Outline each Plasmodium falciparum-infected red blood cell.
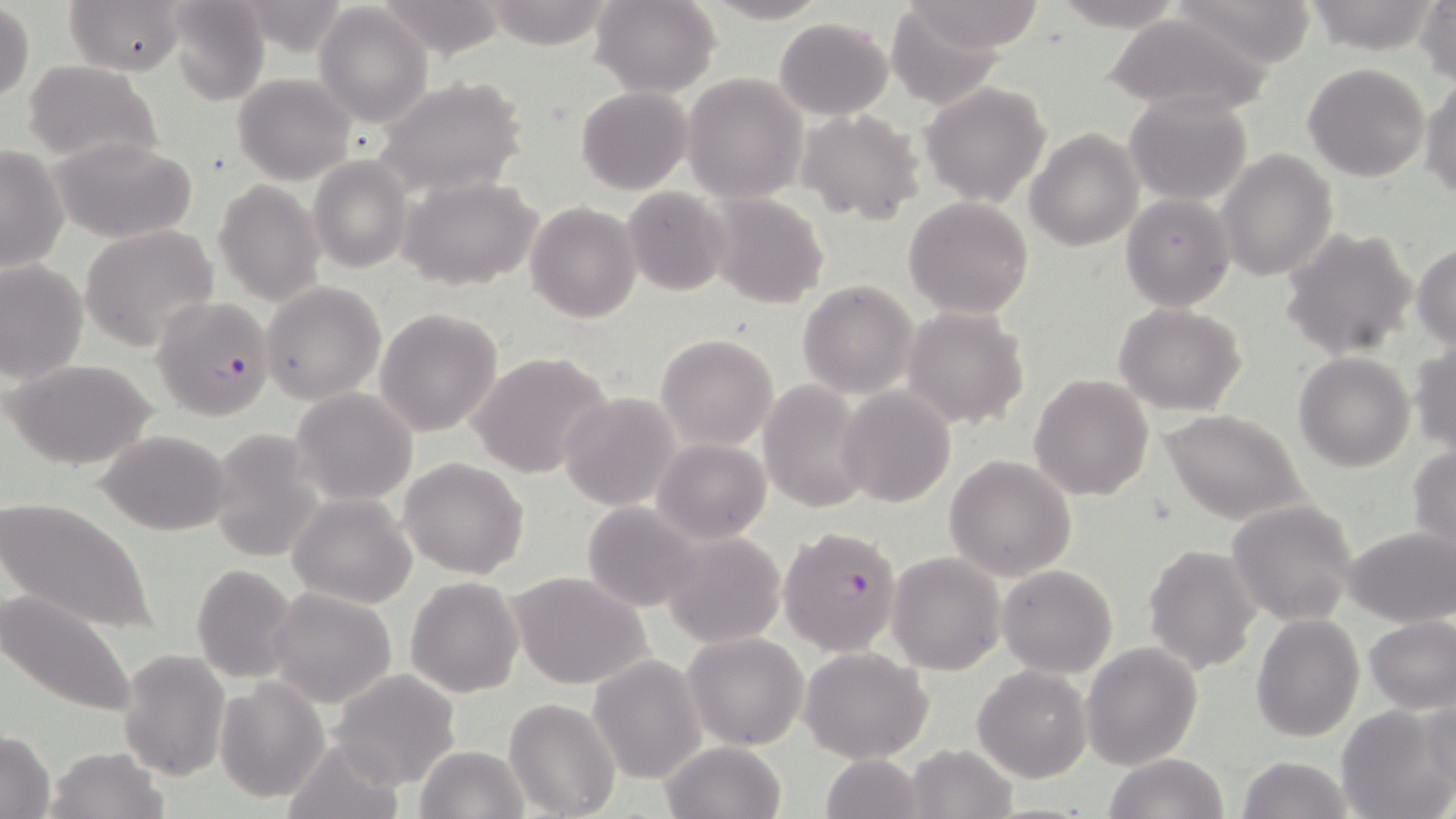
Approximate bounding boxes as [x1, y1, x2, y2] in pixels.
Plasmodium falciparum-infected red blood cells: [149, 296, 275, 422], [778, 525, 902, 656].

Summary:
  - Uninfected red blood cell locations: [64, 0, 185, 77], [165, 0, 270, 106], [481, 0, 615, 49], [590, 0, 720, 98], [703, 0, 830, 24], [1166, 0, 1322, 67], [1301, 0, 1442, 54], [378, 1, 507, 58], [901, 1, 1048, 52], [1416, 1, 1455, 84], [1045, 2, 1191, 31], [233, 3, 354, 53], [886, 3, 1008, 110], [315, 4, 433, 128], [0, 5, 34, 104], [1104, 12, 1271, 117], [773, 17, 894, 119], [24, 60, 162, 168], [1303, 62, 1430, 182], [234, 73, 356, 186], [683, 73, 808, 203], [1421, 73, 1456, 202], [373, 75, 527, 199], [920, 83, 1052, 208], [576, 86, 691, 195], [1125, 92, 1251, 206], [797, 110, 924, 224], [1025, 127, 1144, 251], [50, 137, 199, 243], [0, 144, 69, 272], [1218, 149, 1338, 282], [307, 154, 414, 274], [398, 174, 543, 293], [215, 181, 324, 304], [623, 186, 731, 296], [706, 193, 829, 310], [1121, 193, 1235, 310], [904, 196, 1035, 318], [524, 201, 642, 323], [79, 225, 219, 352], [1280, 226, 1418, 360], [1413, 242, 1456, 346], [0, 259, 88, 387], [798, 280, 918, 398], [260, 281, 386, 406], [1114, 304, 1246, 416], [903, 306, 1031, 429], [373, 307, 503, 437], [656, 334, 779, 451], [1408, 341, 1456, 455], [469, 351, 615, 481], [1294, 352, 1416, 473], [8, 356, 158, 470], [1029, 373, 1154, 501], [758, 380, 869, 512], [837, 386, 956, 507], [291, 387, 419, 505], [558, 392, 683, 512], [1158, 409, 1314, 527], [207, 428, 326, 563], [97, 429, 232, 534], [654, 437, 771, 545], [1407, 444, 1456, 556], [944, 454, 1077, 581], [398, 456, 529, 578], [288, 493, 417, 608], [1, 495, 158, 637], [1227, 498, 1359, 626], [581, 502, 701, 611], [1342, 526, 1454, 627], [659, 529, 787, 648], [1143, 544, 1263, 675], [887, 551, 1006, 675], [191, 565, 298, 683], [998, 565, 1118, 678], [509, 570, 653, 692], [406, 576, 523, 696], [1, 585, 142, 720], [268, 586, 397, 709], [1250, 611, 1363, 742], [1364, 616, 1456, 711], [685, 633, 809, 750], [1081, 641, 1202, 769], [798, 647, 934, 765], [117, 649, 229, 780], [587, 655, 706, 783], [973, 665, 1092, 782], [330, 669, 460, 790], [215, 678, 328, 803], [504, 697, 621, 818], [1419, 697, 1456, 795], [1338, 704, 1454, 819], [0, 731, 55, 818], [281, 738, 403, 818], [661, 741, 787, 819], [906, 744, 1018, 819], [413, 746, 529, 819], [46, 747, 167, 819], [1103, 753, 1229, 819], [818, 754, 924, 819], [1237, 755, 1352, 819]
  - Slide-level diagnosis: Plasmodium falciparum
  - Image size: 1456×819 pixels
  - Preparation: thin blood smear
  - Magnification: 1000x
  - Stain: May-Grünwald-Giemsa
  - Modality: optical microscopy
  - Field of view: single